Identify the parasite.
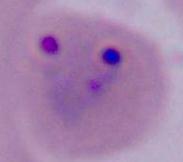
This is Plasmodium.

modality: micrograph
magnification: 400x or 1000x